Locate every Plasmodium vivax-infected red blood cell.
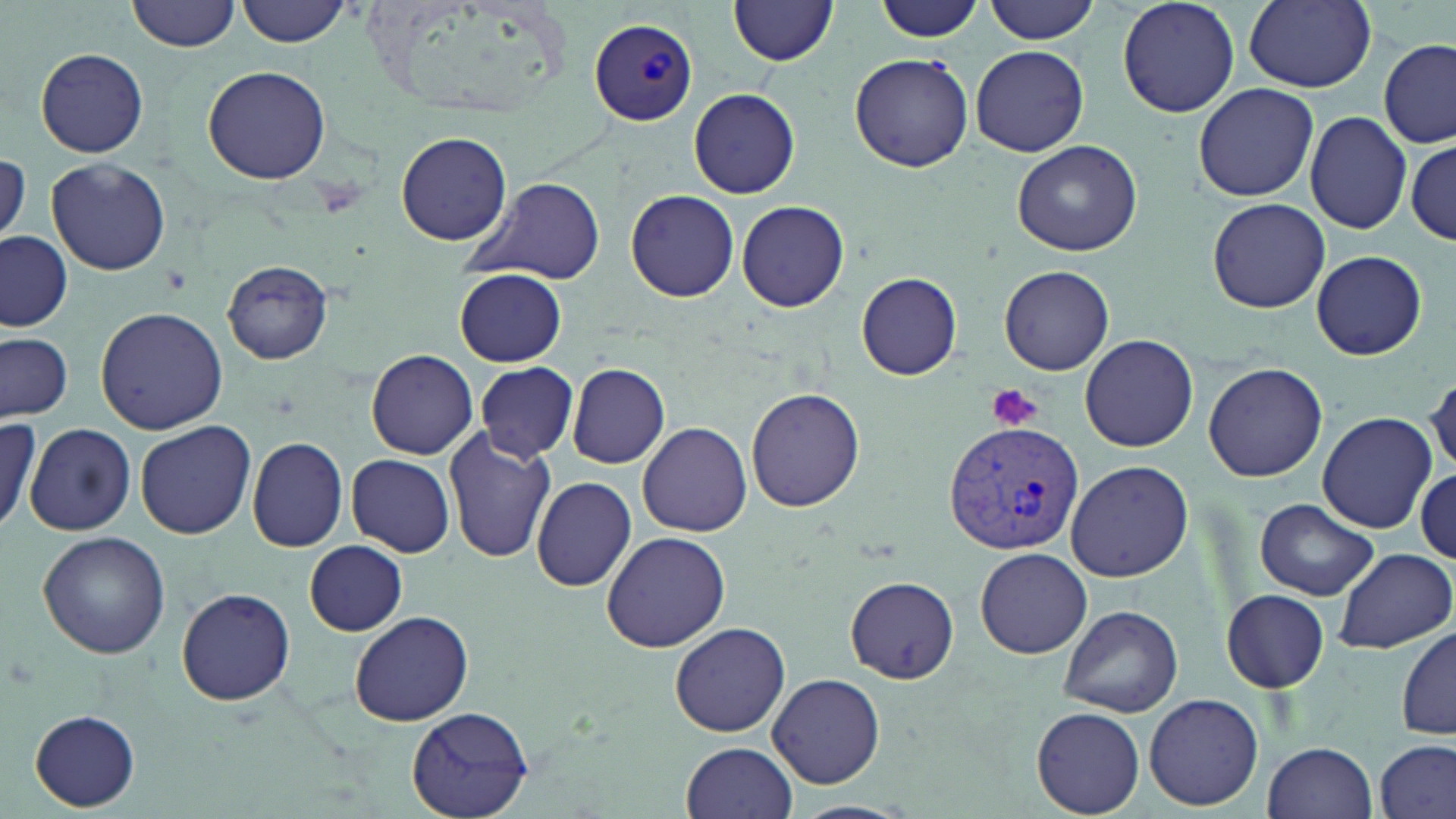
Approximate bounding boxes as [x1, y1, x2, y2] in pixels.
Plasmodium vivax-infected red blood cells: [589, 19, 696, 127], [942, 419, 1084, 557].

slide-level diagnosis = Plasmodium vivax
uninfected red blood cell locations = approximate bounding boxes as [x1, y1, x2, y2] in pixels: [129, 0, 243, 53], [237, 0, 354, 47], [985, 0, 1101, 44], [1116, 0, 1240, 118], [731, 1, 836, 68], [874, 1, 985, 43], [1243, 2, 1376, 91], [1378, 38, 1453, 148], [970, 45, 1089, 157], [36, 48, 148, 158], [851, 53, 974, 172], [201, 65, 332, 185], [1193, 82, 1319, 203], [688, 87, 801, 199], [1305, 111, 1411, 234], [396, 132, 512, 245], [1013, 140, 1143, 256], [1407, 140, 1455, 244], [1, 154, 30, 245], [46, 157, 170, 276], [464, 176, 607, 284], [626, 189, 739, 302], [1207, 197, 1331, 313], [736, 199, 850, 313], [1, 231, 72, 331], [1311, 250, 1429, 361], [223, 260, 331, 364], [1000, 265, 1114, 376], [455, 268, 567, 367], [857, 272, 960, 381], [95, 307, 227, 433], [1079, 333, 1199, 453], [0, 335, 74, 422], [366, 349, 479, 460], [1203, 360, 1328, 483], [476, 363, 578, 460], [567, 363, 671, 469], [1424, 370, 1456, 475], [745, 387, 865, 511], [1317, 413, 1434, 533], [0, 415, 40, 535], [134, 420, 256, 540], [637, 422, 752, 537], [25, 423, 135, 534], [444, 429, 555, 563], [247, 436, 350, 552], [348, 454, 455, 559], [1063, 460, 1194, 582], [1414, 466, 1454, 563], [532, 474, 638, 592], [1254, 498, 1380, 601], [38, 531, 170, 659], [601, 532, 731, 653], [304, 541, 407, 636], [974, 547, 1092, 658], [1333, 548, 1454, 654], [847, 578, 959, 684], [177, 588, 295, 706], [1221, 588, 1330, 693], [1058, 603, 1183, 718], [348, 610, 474, 726], [669, 620, 791, 738], [1395, 625, 1456, 742], [703, 629, 876, 769], [768, 672, 885, 787], [1144, 692, 1265, 810], [407, 707, 533, 819], [1032, 707, 1145, 816], [30, 709, 141, 811], [1375, 739, 1455, 819], [1262, 741, 1378, 819], [681, 742, 798, 819]
preparation = thin blood film
modality = light microscopy
image size = 1456×819 pixels
stain = May-Grünwald-Giemsa
platelet locations = approximate bounding boxes as [x1, y1, x2, y2] in pixels: [987, 383, 1044, 432]
field of view = one of a larger specimen
magnification = 1000x